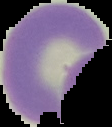

image type = segmented cell region on a black background
image size = 112×127 pixels
preparation = thin blood smear
result = negative for malaria parasites